State the blood parasite species.
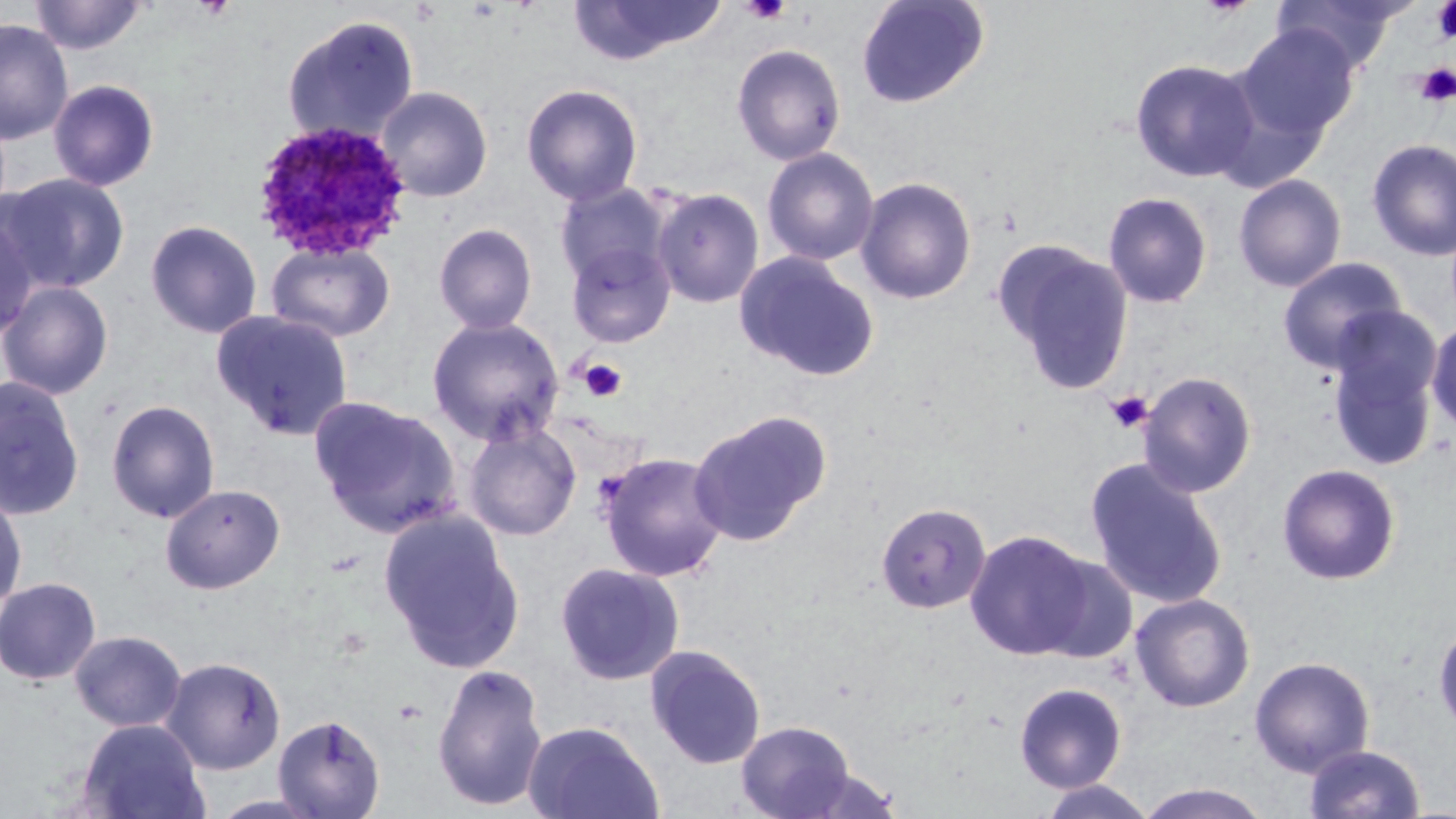
Plasmodium ovale.

Approximate bounding boxes as (x1, y1, x2, y2) in pixels. Plasmodium ovale-infected red blood cell locations: (252, 121, 413, 262). Uninfected red blood cell locations: (29, 0, 148, 56), (856, 0, 990, 109), (567, 1, 727, 66), (1271, 1, 1407, 73), (281, 14, 420, 145), (0, 19, 75, 144), (1236, 24, 1360, 144), (732, 43, 846, 165), (1130, 58, 1260, 183), (48, 78, 161, 192), (521, 83, 643, 206), (375, 85, 493, 202), (1366, 139, 1456, 262), (761, 147, 880, 266), (0, 172, 130, 294), (1233, 174, 1346, 292), (854, 175, 978, 305), (554, 181, 671, 289), (652, 187, 765, 308), (1102, 191, 1213, 309), (0, 213, 40, 344), (145, 219, 263, 339), (433, 223, 538, 335), (564, 239, 677, 349), (265, 240, 396, 343), (994, 241, 1135, 396), (733, 251, 881, 382), (1277, 257, 1407, 373), (0, 279, 114, 400), (211, 309, 355, 439), (1324, 309, 1443, 472), (426, 315, 565, 446), (1426, 317, 1456, 435), (1138, 371, 1257, 497), (0, 376, 85, 522), (309, 395, 461, 537), (105, 398, 220, 523), (688, 410, 832, 546), (463, 422, 582, 541), (597, 451, 729, 582), (1085, 458, 1228, 609), (1277, 463, 1402, 585), (160, 483, 286, 594), (0, 488, 27, 613), (875, 501, 992, 614), (378, 507, 525, 673), (964, 529, 1095, 660), (1035, 553, 1139, 664), (554, 561, 685, 685), (0, 577, 101, 685), (1130, 593, 1256, 712), (1433, 619, 1456, 739), (69, 630, 186, 732), (644, 644, 767, 769), (1249, 655, 1375, 777), (161, 656, 286, 774), (431, 662, 549, 811), (1014, 682, 1127, 793), (272, 713, 386, 818), (77, 718, 211, 819), (523, 719, 664, 819), (734, 719, 858, 819), (1303, 744, 1426, 818), (1035, 779, 1158, 818), (1133, 782, 1276, 818). Platelet locations: (740, 0, 791, 24), (1431, 1, 1456, 45), (1416, 63, 1456, 107), (579, 358, 627, 402), (1105, 390, 1153, 434). May-Grünwald-Giemsa stain. Thin blood film. Image is 1456×819 pixels. One field of a larger specimen. 1000x magnification. Light microscopy.